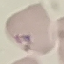 Result: negative for malaria parasites. Thin blood film. Photographed with a smartphone camera at the microscope eyepiece. Automatically extracted cell patch, resized to 64 × 64 pixels. Giemsa-stained preparation.